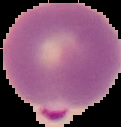
image type = cell region segmented out of the field of view; surrounding area masked to black
result = Plasmodium parasites detected
preparation = thin blood smear
image size = 121×127 pixels